Describe the morphology of the red blood cells.
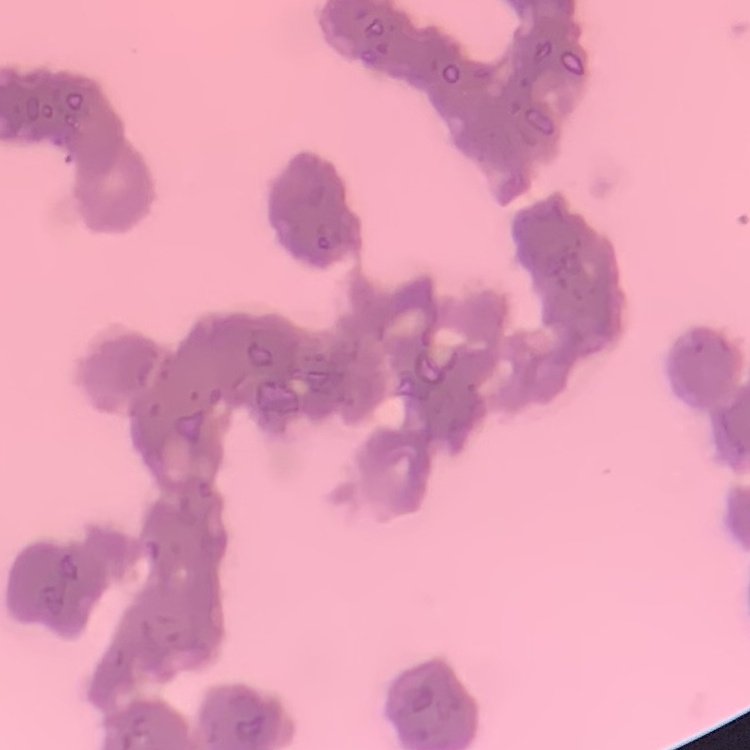

They show rouleaux formation.

Thin blood film. Square crop of a larger photomicrograph. Stained with either Field's or Giemsa.